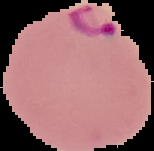

Summary:
  - Image type: segmented cell region with the area outside set to black
  - Preparation: thin blood smear
  - Image size: 154×151 pixels
  - Result: malaria parasites detected